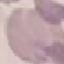
Summary:
  - Malaria status: uninfected
  - Preparation: thin blood smear
  - Stain: Giemsa
  - Capture: smartphone camera at the microscope eyepiece
  - Image type: cell patch, automatically extracted from a larger field of view and resized to 64 × 64 pixels